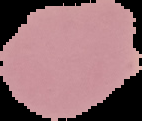
preparation = thin blood smear
image size = 142×121 pixels
image type = segmented cell region on a black background
result = no Plasmodium parasites seen